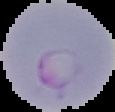
Summary:
  - Result: malaria parasites detected
  - Preparation: thin blood film
  - Image type: segmented cell region with the area outside set to black
  - Image size: 115×112 pixels